Locate the red blood cells and classify each one as Plasmodium falciparum-infected, uninfected, or of indeterminate infection status.
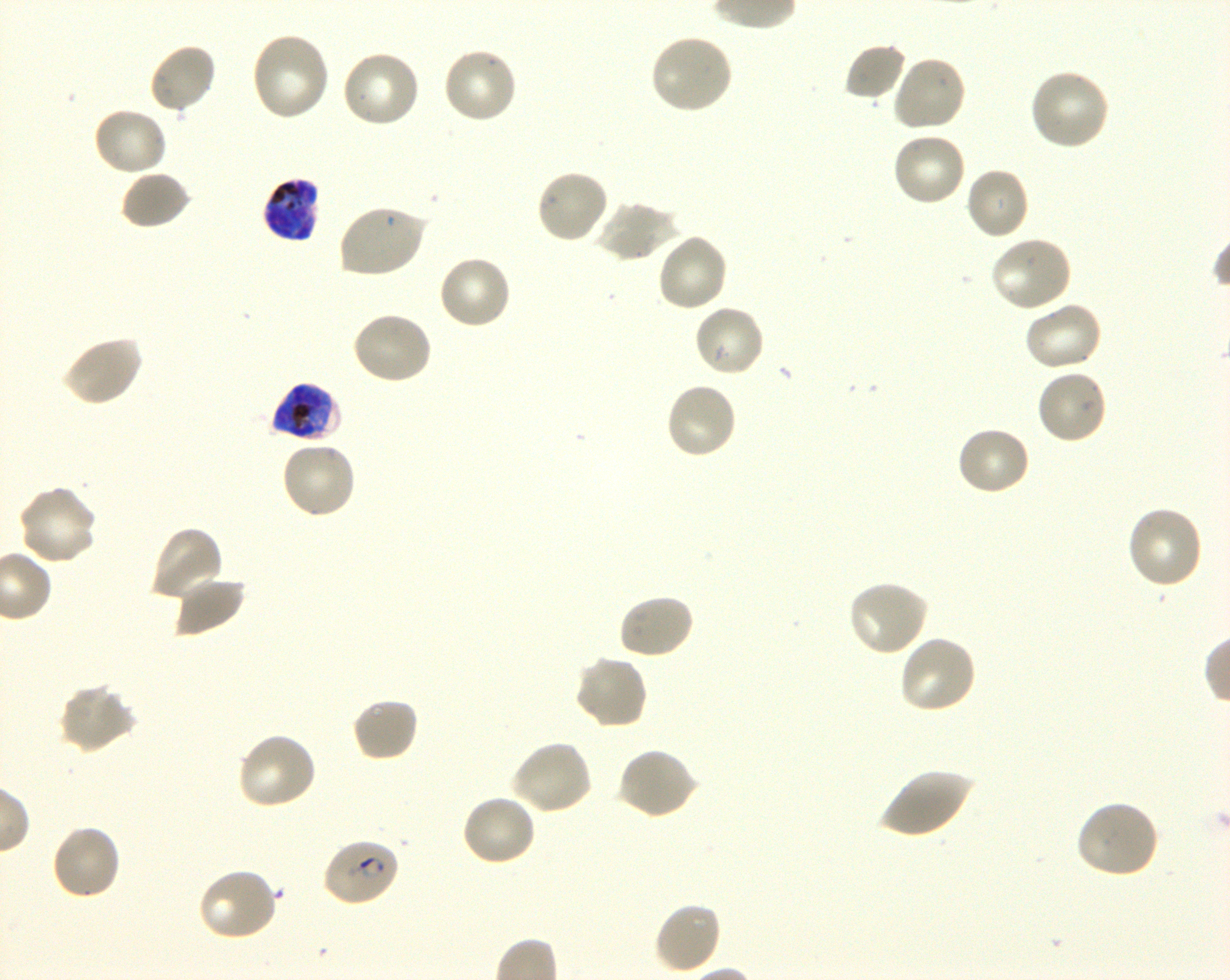

Approximate bounding boxes as [x1, y1, x2, y2] in pixels. Not every red blood cell is marked. A life-cycle stage — or a range of stages, where the recorded stages span more than one — follows each staged infected red blood cell.
Infected red blood cells: [263, 176, 321, 243] late trophozoite to late schizont; [269, 382, 340, 444] late trophozoite to late schizont; [321, 838, 400, 908] early ring to early trophozoite.
Uninfected red blood cells: [249, 31, 330, 122], [649, 32, 733, 115], [148, 42, 218, 116], [843, 42, 907, 102], [442, 46, 519, 124], [340, 49, 421, 129], [891, 54, 967, 133], [1028, 68, 1111, 152], [92, 106, 169, 177], [892, 132, 967, 207], [965, 166, 1030, 240], [535, 168, 610, 245], [119, 170, 192, 230], [594, 200, 679, 262], [337, 203, 428, 279], [656, 232, 729, 313], [989, 236, 1074, 314], [437, 254, 514, 331], [1023, 301, 1103, 372], [693, 303, 767, 377], [350, 309, 434, 386], [60, 334, 143, 408], [1035, 368, 1109, 445], [664, 381, 739, 461], [956, 426, 1032, 498], [280, 439, 358, 520], [17, 484, 99, 566], [1126, 505, 1205, 590], [149, 525, 225, 603], [173, 576, 247, 638], [847, 579, 928, 658], [618, 593, 696, 660], [897, 634, 978, 715], [573, 654, 650, 730], [58, 683, 138, 754], [350, 697, 420, 764], [236, 731, 318, 811], [510, 739, 594, 816], [616, 748, 699, 821], [878, 767, 973, 840], [460, 792, 536, 866], [1075, 799, 1161, 880], [49, 823, 122, 901], [196, 867, 279, 943], [653, 901, 722, 975].
No red blood cells of indeterminate infection status observed.

donor_blood_group: O+
field_of_view: single
image_size: 1230×980 pixels
stain: Giemsa
objective: 100x, oil immersion, numerical aperture 1.30
preparation: thin blood film
culture: Plasmodium falciparum strain 3D7, shaking, in vitro